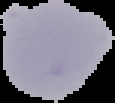

preparation = thin blood film
result = no Plasmodium parasites detected
image size = 115×103 pixels
image type = cell region segmented out of the field of view; surrounding area masked to black